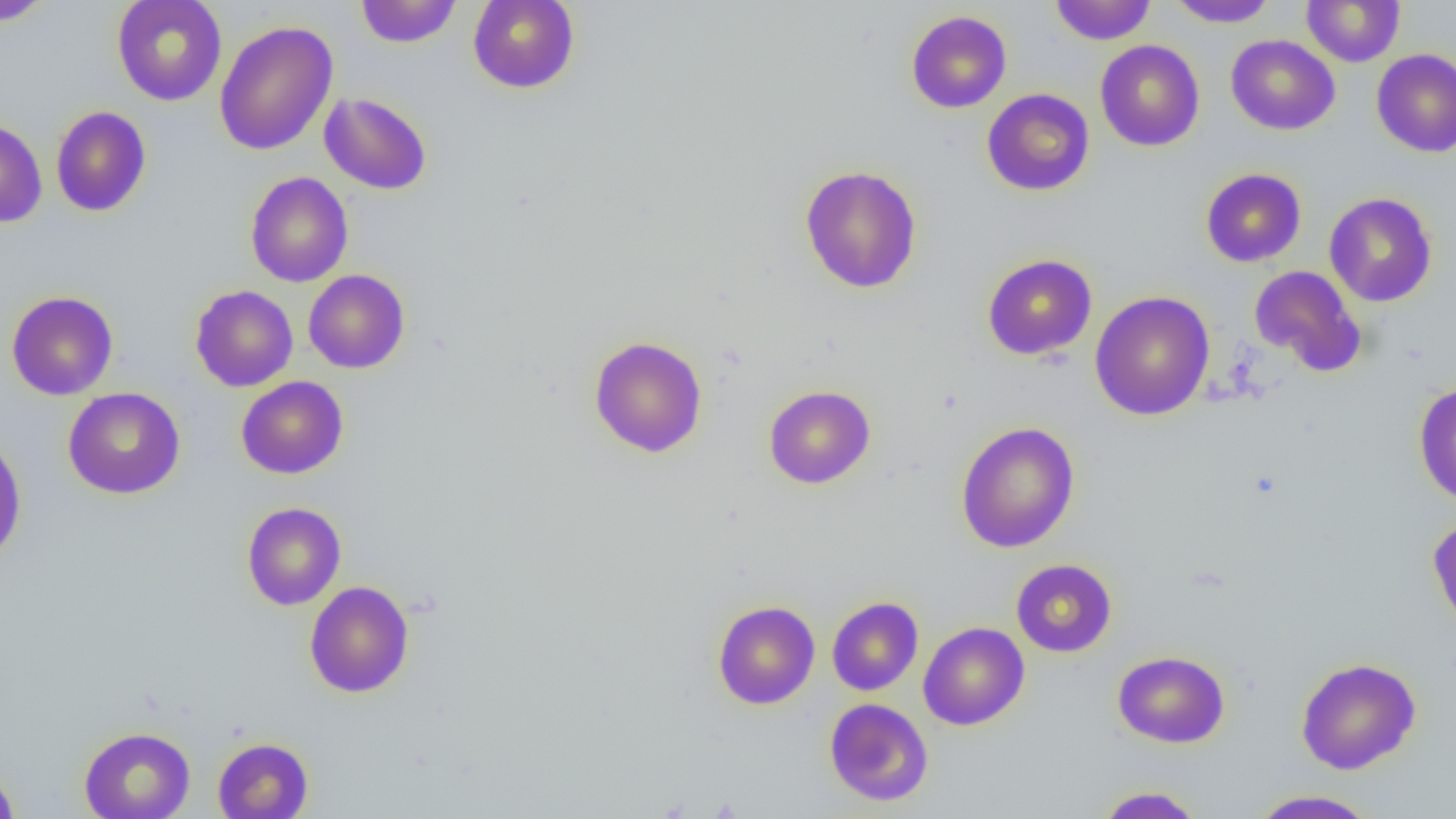
slide-level diagnosis = no evidence of blood parasites
uninfected red blood cell locations = approximate bounding boxes as named x1/y1/x2/y2 corners in pixels: (x1=1, y1=0, x2=54, y2=26), (x1=112, y1=0, x2=227, y2=106), (x1=355, y1=0, x2=461, y2=48), (x1=1050, y1=0, x2=1155, y2=44), (x1=1166, y1=0, x2=1279, y2=28), (x1=467, y1=1, x2=580, y2=94), (x1=1301, y1=1, x2=1405, y2=67), (x1=906, y1=10, x2=1012, y2=113), (x1=214, y1=20, x2=338, y2=155), (x1=1226, y1=35, x2=1340, y2=135), (x1=1095, y1=40, x2=1205, y2=152), (x1=1371, y1=48, x2=1456, y2=157), (x1=982, y1=88, x2=1095, y2=196), (x1=319, y1=91, x2=432, y2=195), (x1=51, y1=106, x2=151, y2=217), (x1=0, y1=118, x2=47, y2=227), (x1=799, y1=165, x2=922, y2=293), (x1=1201, y1=168, x2=1307, y2=267), (x1=245, y1=171, x2=354, y2=287), (x1=1324, y1=192, x2=1437, y2=307), (x1=982, y1=254, x2=1097, y2=360), (x1=1249, y1=265, x2=1366, y2=377), (x1=303, y1=269, x2=410, y2=373), (x1=190, y1=285, x2=298, y2=391), (x1=6, y1=290, x2=119, y2=400), (x1=1090, y1=290, x2=1215, y2=421), (x1=589, y1=336, x2=707, y2=458), (x1=236, y1=376, x2=348, y2=479), (x1=1413, y1=381, x2=1456, y2=506), (x1=763, y1=384, x2=875, y2=489), (x1=63, y1=387, x2=185, y2=499), (x1=956, y1=421, x2=1080, y2=553), (x1=0, y1=432, x2=27, y2=565), (x1=241, y1=502, x2=346, y2=610), (x1=1427, y1=516, x2=1456, y2=636), (x1=1011, y1=559, x2=1116, y2=657), (x1=304, y1=580, x2=414, y2=698), (x1=827, y1=597, x2=924, y2=696), (x1=712, y1=600, x2=820, y2=709), (x1=918, y1=622, x2=1030, y2=730), (x1=1113, y1=650, x2=1230, y2=748), (x1=1295, y1=657, x2=1421, y2=774), (x1=824, y1=698, x2=933, y2=806), (x1=79, y1=727, x2=195, y2=819), (x1=212, y1=737, x2=313, y2=818), (x1=0, y1=763, x2=20, y2=818), (x1=1094, y1=786, x2=1205, y2=818), (x1=1247, y1=790, x2=1381, y2=818)
magnification = 1000x
preparation = thin blood smear
modality = light microscopy
field of view = single
image size = 1456×819 pixels